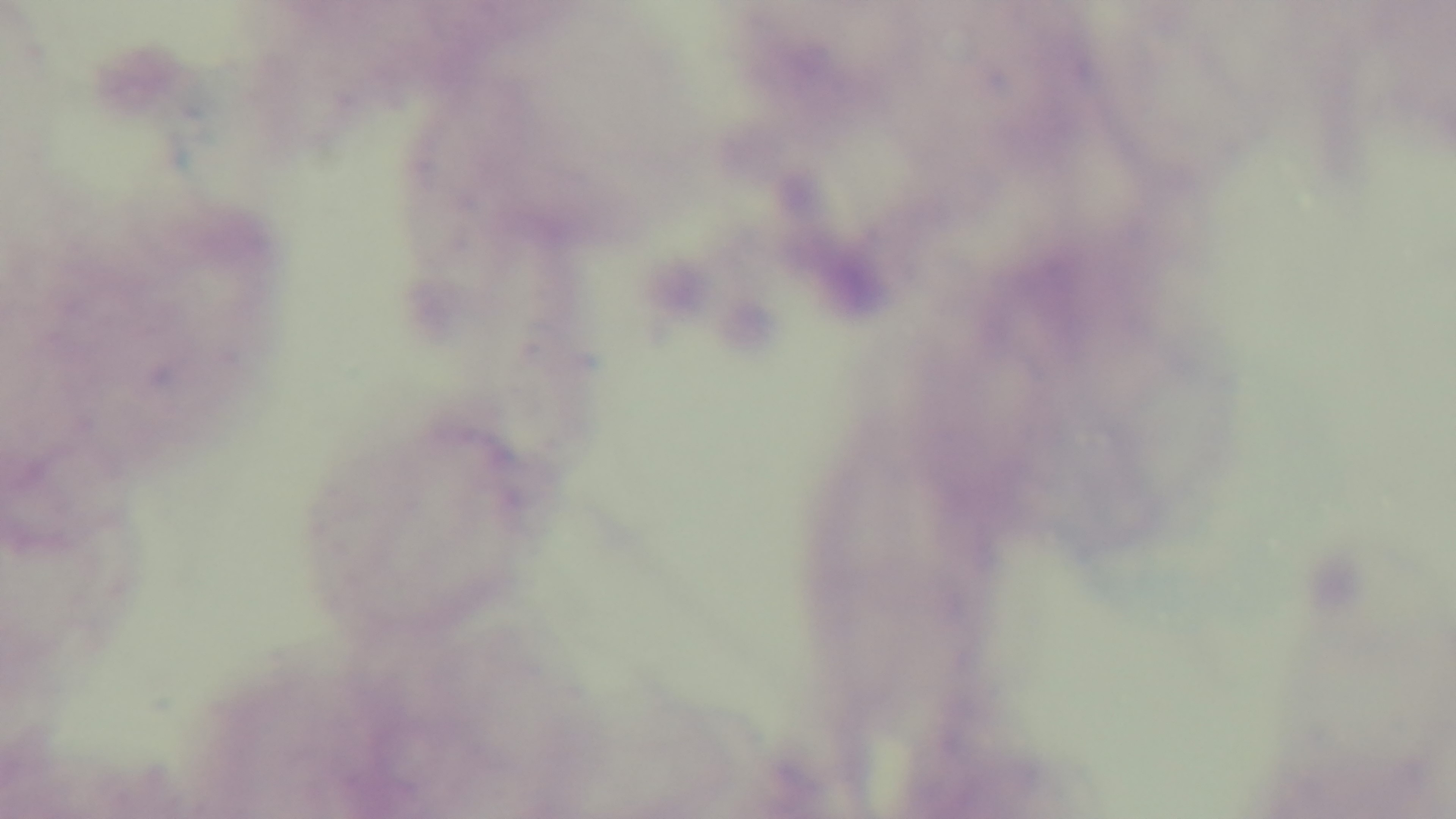 Single field of view. Light microscopy. Malaria status: uninfected. Preparation: thick smear. 100x oil-immersion objective. Captured with a mounted 4K digital camera. Giemsa-stained.